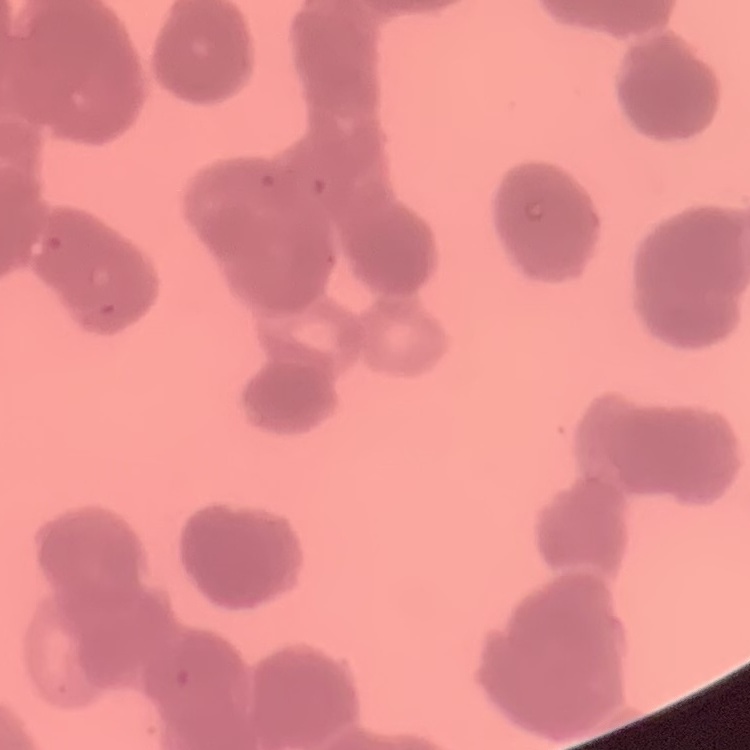

{
  "red_blood_cell_morphology": "rouleaux formation",
  "preparation": "thin peripheral smear",
  "image_type": "one tile cut from a larger photomicrograph",
  "stain": "Field's or Giemsa"
}